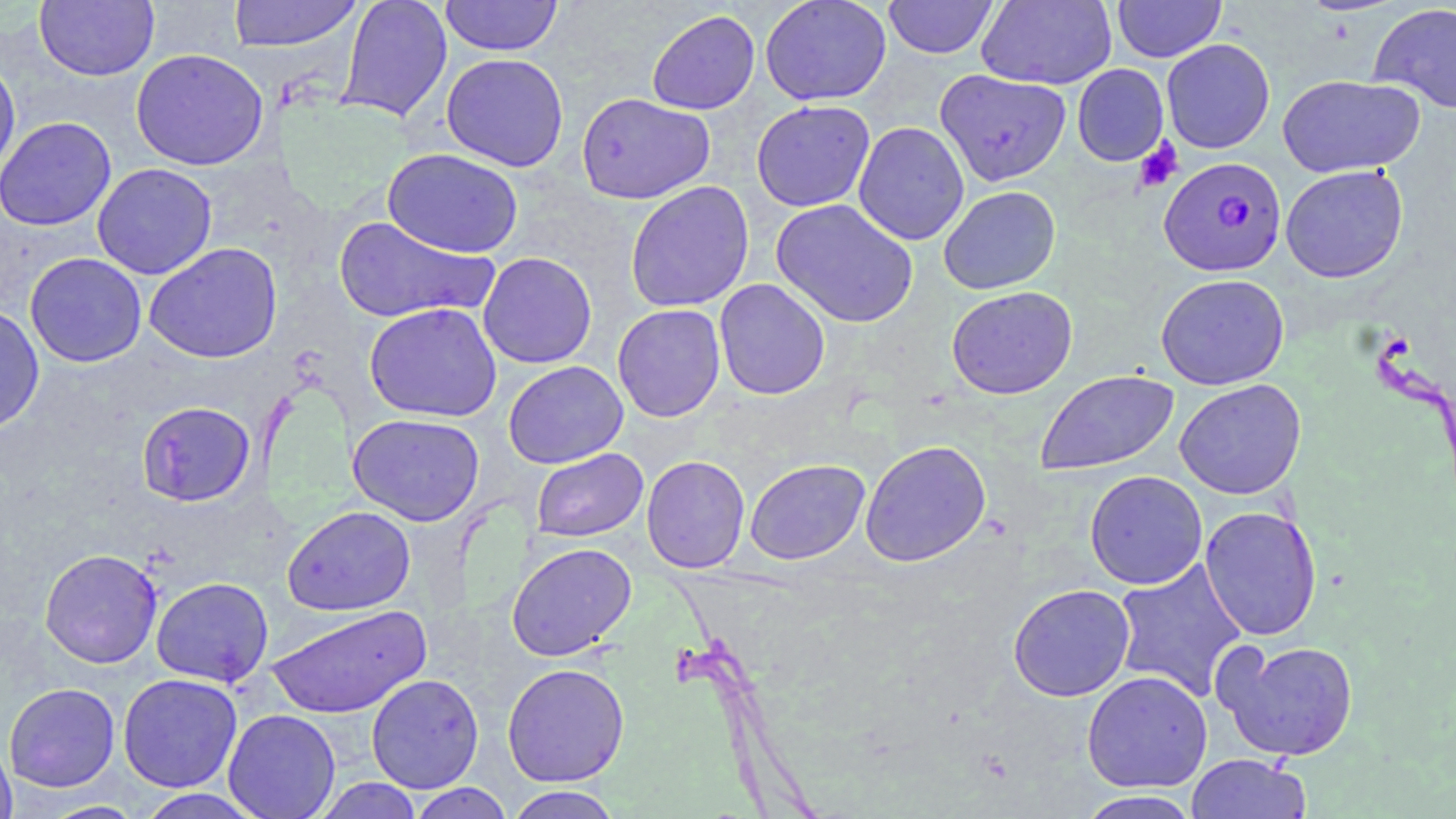
Summary:
  - Coordinate format: approximate bounding boxes as [x1, y1, x2, y2] in pixels
  - Uninfected red blood cell locations: [35, 0, 159, 81], [228, 0, 362, 51], [337, 0, 452, 122], [440, 0, 562, 56], [759, 0, 892, 106], [883, 0, 998, 59], [977, 0, 1117, 89], [1112, 0, 1226, 62], [1368, 3, 1456, 114], [646, 10, 760, 114], [1161, 38, 1275, 154], [130, 49, 269, 171], [441, 53, 569, 172], [0, 59, 21, 182], [1072, 64, 1169, 166], [935, 69, 1071, 186], [1278, 73, 1425, 178], [576, 92, 715, 204], [751, 100, 875, 212], [0, 116, 116, 231], [853, 121, 969, 245], [382, 148, 524, 258], [92, 162, 217, 280], [1279, 164, 1408, 283], [625, 181, 754, 313], [938, 185, 1060, 295], [771, 198, 919, 328], [333, 215, 499, 324], [144, 243, 283, 363], [25, 252, 147, 368], [478, 252, 597, 369], [1155, 273, 1290, 390], [714, 278, 831, 400], [946, 286, 1078, 399], [364, 302, 502, 422], [0, 304, 44, 433], [612, 304, 726, 422], [503, 361, 628, 468], [1035, 370, 1178, 475], [1174, 379, 1306, 499], [137, 400, 255, 506], [348, 413, 485, 526], [859, 440, 992, 567], [531, 448, 648, 542], [641, 455, 750, 573], [744, 458, 870, 564], [1084, 470, 1207, 589], [283, 505, 415, 616], [1199, 505, 1323, 641], [506, 542, 636, 661], [39, 548, 163, 668], [1111, 559, 1247, 701], [151, 577, 274, 687], [1007, 583, 1136, 702], [265, 604, 432, 719], [1215, 639, 1360, 761], [317, 641, 471, 769], [502, 662, 630, 786], [1081, 670, 1212, 793], [117, 673, 242, 792], [366, 673, 484, 793], [4, 682, 120, 792], [223, 708, 340, 819], [0, 735, 17, 819], [1186, 753, 1310, 819], [313, 778, 423, 818], [407, 783, 515, 819], [505, 786, 622, 818], [135, 789, 267, 819], [1075, 790, 1202, 819], [39, 800, 147, 818]
  - Platelet locations: [1133, 138, 1183, 193]
  - Plasmodium falciparum-infected red blood cell locations: [1158, 157, 1286, 277]
  - Slide-level diagnosis: Plasmodium falciparum
  - Magnification: 1000x
  - Stain: May-Grünwald-Giemsa
  - Modality: optical microscopy
  - Image size: 1456×819 pixels
  - Preparation: thin blood smear
  - Field of view: single